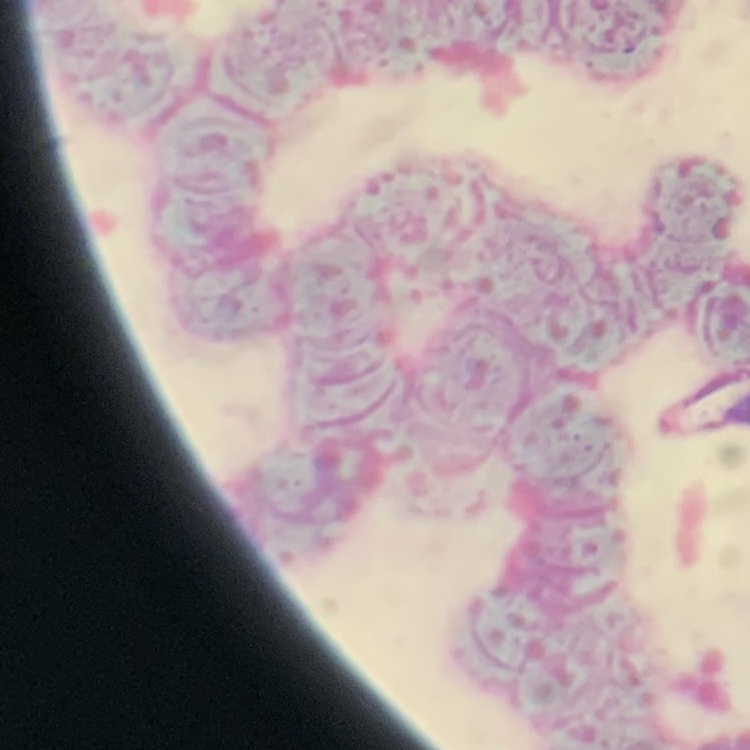

Summary:
  - Erythrocyte morphology: rouleaux formation
  - Stain: Field's or Giemsa
  - Image type: one tile cut from a larger photomicrograph
  - Preparation: thin blood smear